Describe the morphology of the erythrocytes.
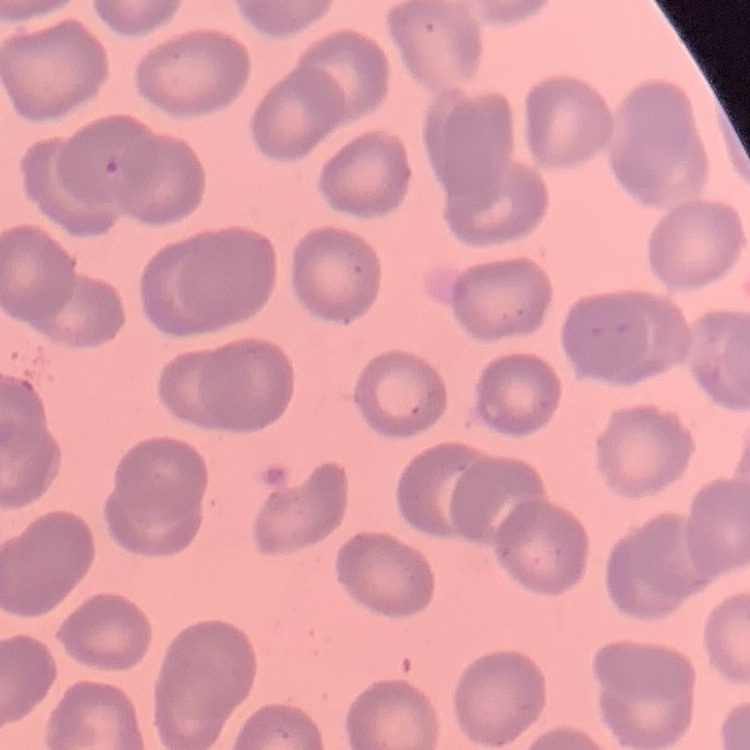
They show no rouleaux formation.

Summary:
  - Stain: Field's or Giemsa
  - Image type: square crop of a larger photomicrograph
  - Preparation: thin peripheral smear